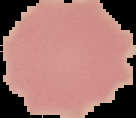
Summary:
  - Image size: 136×118 pixels
  - Result: no malaria parasites seen
  - Image type: cell region segmented out of the field of view; surrounding area masked to black
  - Preparation: thin blood film